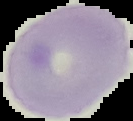
From a thin blood smear. Image is 133×121 pixels. The area outside the segmented cell region is set to black. Result: no malaria parasites detected.